Report the malaria status of this cell.
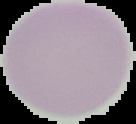

Uninfected.

Image is 136×124 pixels. Cell region segmented out of the field of view; the surrounding area is masked to black. From a thin blood film.